Evaluate for malaria.
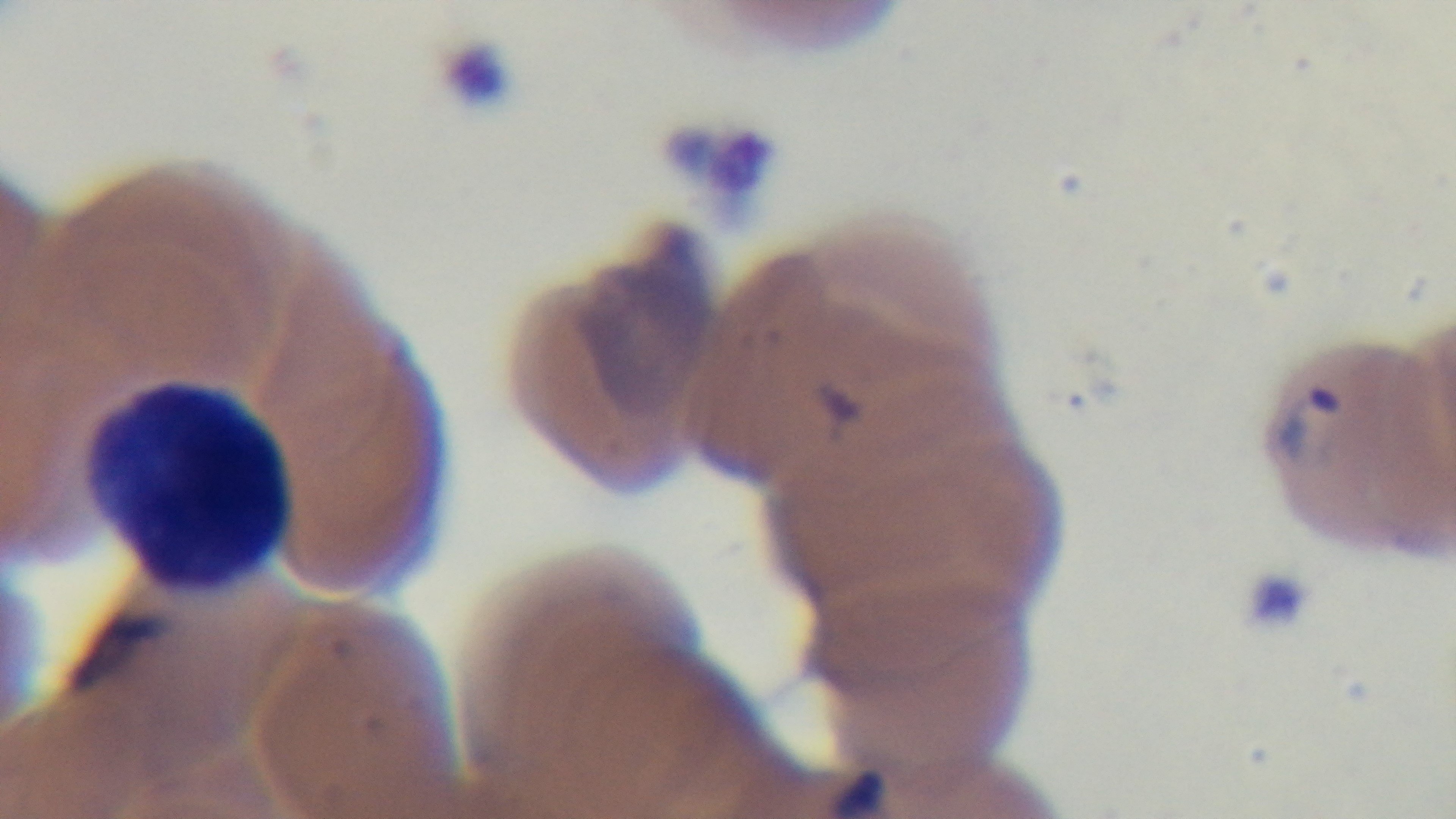

It is infected.

Oil-immersion objective, 100x. Mounted 4K digital camera. Preparation: thin. One field from the slide. Giemsa stain. Photomicrograph.